Give a bounding box for every malaria parasite, every leukocyte, and every artifact (stain precipitate or debris).
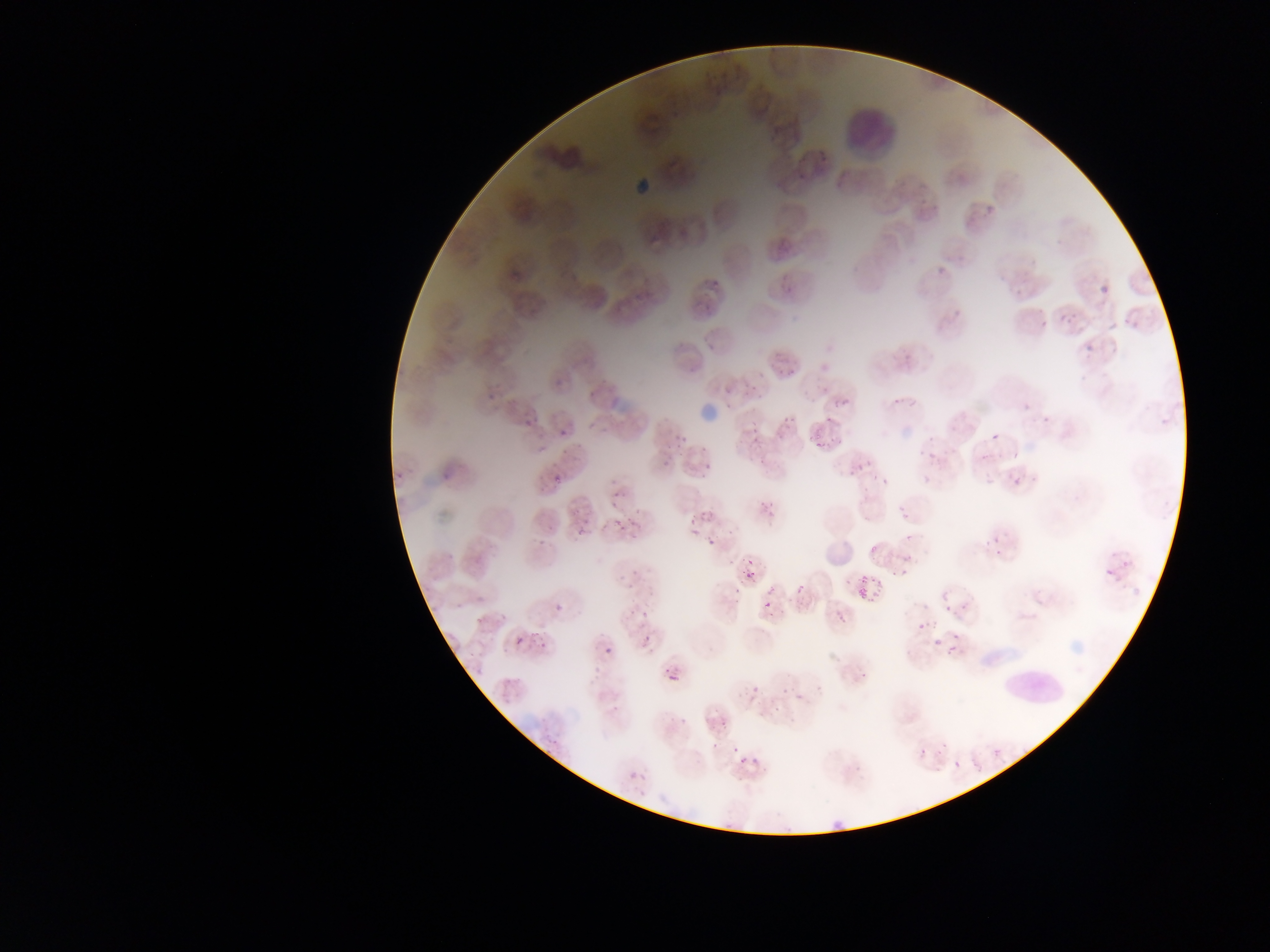

Approximate bounding boxes as left top right bottom in pixels.
Malaria parasites: 793 170 805 182; 932 258 949 278; 779 269 796 294; 705 276 723 297; 1102 285 1110 294; 692 294 713 307; 950 299 963 320; 1061 316 1075 328; 1033 318 1046 332; 1082 335 1096 355; 487 361 520 408; 592 364 612 391; 774 365 800 385; 550 367 565 383; 891 385 910 408; 718 389 739 410; 825 397 844 415; 1023 404 1030 412; 585 411 606 432; 514 412 535 426; 779 419 807 440; 742 427 760 438; 552 429 569 443; 823 431 850 455; 669 432 686 453; 990 433 998 442; 741 437 762 452; 924 445 940 460; 657 449 682 466; 387 460 409 479; 698 461 712 476; 850 465 865 476; 880 466 892 491; 915 469 934 486; 1007 473 1019 489; 548 474 566 491; 861 474 878 486; 602 485 614 501; 631 501 654 518; 895 503 912 518; 749 504 775 523; 613 507 634 534; 695 517 708 527; 572 518 598 535; 984 523 1007 550; 537 524 551 536; 901 528 920 542; 865 534 887 559; 701 535 722 549; 1100 551 1127 581; 895 554 921 580; 621 558 648 593; 736 570 751 588; 789 572 822 598; 851 579 872 586; 550 589 579 614; 856 589 863 599; 762 599 773 609; 940 599 962 620; 619 604 638 616; 834 613 850 630; 916 615 925 627; 468 621 487 637; 526 627 550 658; 622 627 661 645; 510 632 530 648; 946 638 963 659; 602 646 610 656; 468 653 489 677; 848 660 873 685; 667 672 679 682; 744 690 752 706; 786 693 801 705; 711 701 736 730; 916 725 945 767; 732 746 777 769; 993 750 1000 758; 626 771 636 780 | approximate x y pixel centers of objects too small to bound: 932 640.
Leukocytes: 839 105 899 158; 998 666 1068 711.

image_size: 1270×952 pixels
country: Ghana
preparation: thin blood film
capture: mobile-phone photograph through a microscope
field_of_view: single